Locate platelets.
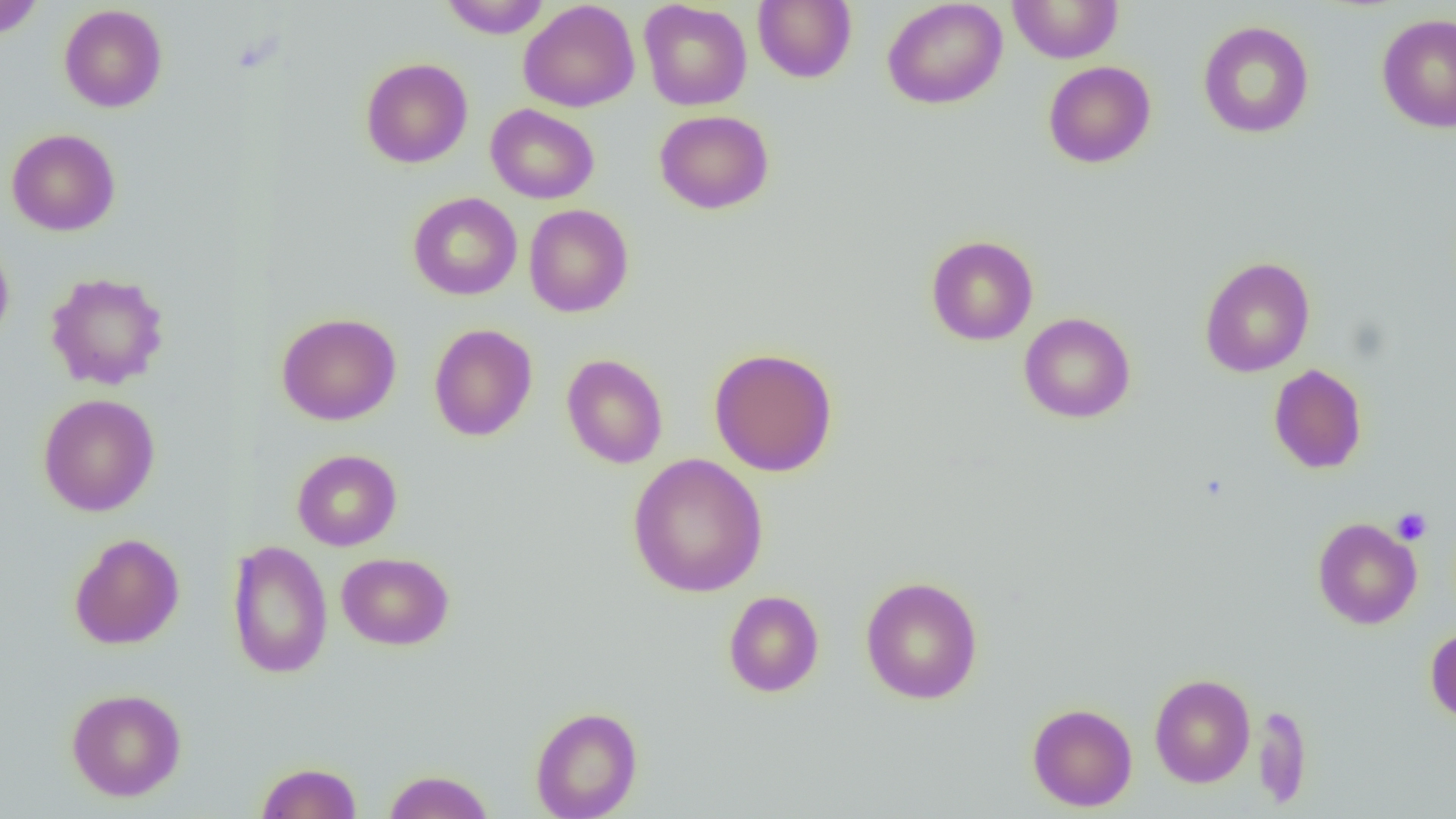

Approximate bounding boxes as [x1, y1, x2, y2] in pixels.
Platelets: [1391, 507, 1432, 545].

Uninfected red blood cell locations: [0, 0, 45, 40], [440, 0, 551, 38], [753, 0, 857, 83], [882, 0, 1007, 109], [1007, 0, 1124, 64], [518, 1, 640, 112], [639, 1, 752, 110], [59, 4, 168, 112], [1376, 13, 1456, 134], [1198, 21, 1314, 139], [360, 58, 473, 168], [1043, 61, 1156, 168], [486, 104, 599, 204], [654, 109, 775, 214], [7, 129, 120, 236], [408, 192, 522, 300], [523, 204, 634, 317], [925, 235, 1039, 345], [0, 237, 14, 346], [1200, 256, 1315, 378], [45, 271, 170, 390], [276, 312, 401, 426], [1019, 312, 1136, 424], [428, 323, 538, 442], [708, 347, 839, 476], [561, 354, 668, 469], [1268, 364, 1368, 474], [38, 393, 160, 516], [292, 449, 402, 551], [627, 453, 768, 598], [1312, 517, 1422, 629], [69, 533, 185, 650], [227, 539, 333, 679], [228, 545, 453, 661], [336, 552, 454, 650], [859, 575, 984, 705], [723, 590, 824, 697], [1425, 627, 1456, 724], [1149, 673, 1255, 787], [66, 688, 186, 801], [1027, 702, 1137, 811], [1253, 704, 1313, 810], [530, 706, 643, 819], [255, 762, 363, 819], [382, 769, 495, 819]. Slide-level diagnosis: no evidence of blood parasites. 1000x magnification. Image is 1456×819 pixels. One field of a larger specimen. Optical microscopy. Thin blood smear.